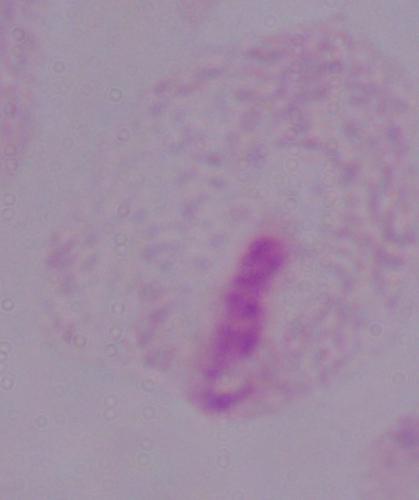

A trichomonad is shown. Captured at 1000x magnification. Photomicrograph.